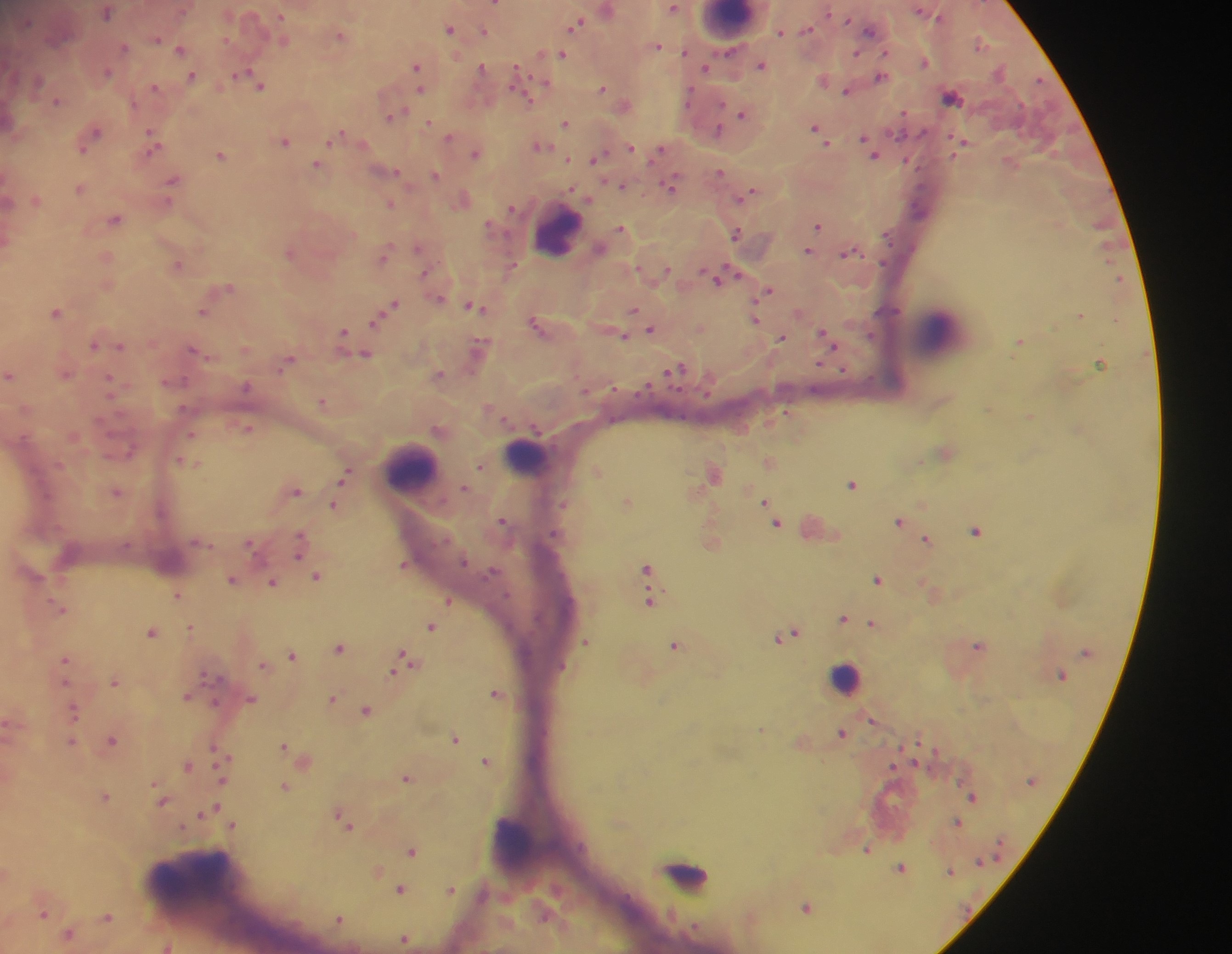

Approximate centers as (x, y) in pixels. Leukocyte locations: (728, 22), (565, 233), (930, 336), (525, 458), (408, 464), (845, 684), (517, 844), (183, 885). Malaria parasite locations: (674, 9), (828, 12), (282, 16), (577, 22), (450, 26), (484, 29), (871, 29), (781, 34), (341, 35), (157, 38), (179, 48), (727, 51), (886, 51), (562, 52), (857, 52), (541, 53), (417, 65), (481, 65), (517, 66), (705, 67), (545, 82), (260, 86), (419, 88), (602, 88), (692, 88), (522, 94), (953, 98), (722, 103), (1021, 105), (742, 113), (389, 118), (429, 120), (566, 122), (815, 126), (718, 128), (95, 131), (150, 131), (921, 133), (866, 138), (963, 140), (328, 141), (286, 142), (156, 144), (630, 145), (83, 150), (605, 150), (473, 152), (601, 152), (221, 154), (567, 157), (592, 159), (317, 164), (719, 170), (919, 170), (394, 171), (436, 175), (173, 179), (669, 186), (572, 188), (738, 198), (510, 206), (820, 225), (619, 229), (735, 233), (418, 248), (808, 250), (847, 252), (881, 264), (177, 265), (512, 266), (424, 273), (736, 273), (717, 278), (767, 291), (391, 306), (477, 306), (634, 309), (55, 312), (204, 312), (1082, 315), (756, 319), (370, 327), (652, 327), (344, 330), (625, 335), (869, 335), (782, 338), (344, 339), (1019, 340), (120, 344), (95, 345), (193, 349), (365, 353), (818, 363), (1099, 363), (284, 364), (681, 364), (668, 370), (10, 375), (109, 375), (186, 380), (871, 380), (649, 382), (613, 386), (588, 390), (321, 401), (787, 411), (250, 427), (533, 429), (192, 435), (180, 459), (185, 461), (479, 465), (598, 469), (716, 473), (343, 479), (853, 484), (298, 490), (118, 492), (764, 500), (334, 503), (564, 503), (502, 520), (900, 520), (777, 523), (976, 530), (302, 533), (927, 538), (298, 556), (465, 562), (404, 564), (648, 567), (878, 578), (273, 581), (178, 595), (651, 602), (449, 603), (843, 619), (872, 622), (190, 625), (432, 627), (151, 631), (795, 631), (781, 637), (587, 641), (674, 644), (979, 644), (341, 649), (404, 653), (1082, 654), (291, 655), (65, 658), (262, 665), (205, 673), (393, 674), (1065, 679), (67, 681), (115, 683), (496, 691), (189, 698), (333, 699), (215, 703), (74, 706), (365, 710), (6, 720), (873, 720), (842, 733), (455, 740), (113, 741), (72, 742), (284, 745), (215, 747), (229, 758), (915, 759), (486, 760), (188, 765), (407, 778), (1031, 780), (221, 781), (154, 782), (285, 787), (968, 794), (105, 796), (164, 801), (217, 805), (337, 812), (203, 814), (958, 820), (234, 824), (183, 827), (352, 827), (412, 851), (998, 856), (979, 861), (898, 868), (949, 875), (401, 888), (452, 889), (806, 905), (43, 914), (108, 916), (336, 918), (68, 933), (403, 940). Thick blood film. Collected in Ghana. Photographed through a microscope with a mobile-phone camera. Image is 1232×954 pixels. Single field of view.